Name the cell type shown.
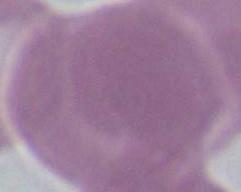
This is an erythrocyte.

Summary:
  - Magnification: 1000x
  - Modality: micrograph